Locate every blood parasite and identify its species.
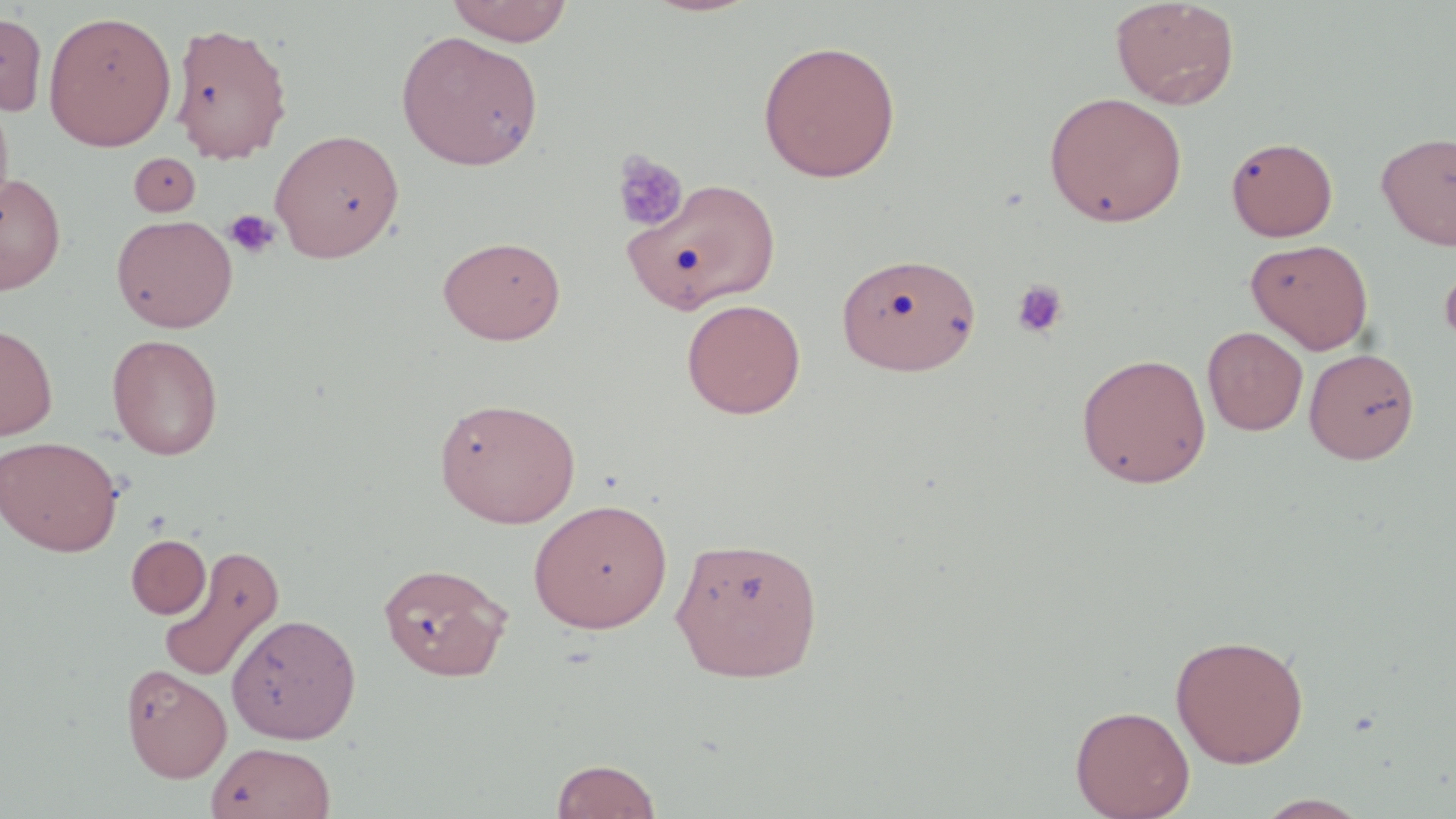
No blood parasites observed.

Summary:
  - Coordinate format: approximate bounding boxes as [x1, y1, x2, y2] in pixels
  - Uninfected red blood cell locations: [446, 0, 573, 46], [1109, 0, 1241, 110], [44, 10, 176, 151], [0, 12, 48, 116], [170, 21, 293, 163], [396, 30, 544, 170], [758, 40, 902, 183], [1043, 91, 1188, 228], [0, 92, 14, 218], [270, 128, 404, 263], [1376, 131, 1456, 251], [1225, 136, 1338, 241], [129, 152, 201, 216], [0, 172, 66, 294], [622, 176, 782, 313], [112, 214, 238, 333], [437, 235, 566, 345], [1245, 238, 1374, 354], [836, 252, 981, 376], [1438, 252, 1456, 351], [681, 298, 806, 419], [0, 322, 58, 440], [1202, 326, 1308, 436], [107, 333, 223, 460], [1304, 348, 1419, 463], [1076, 352, 1212, 489], [433, 396, 581, 528], [0, 435, 123, 556], [529, 498, 673, 633], [670, 533, 824, 683], [126, 534, 211, 618], [158, 544, 285, 682], [378, 561, 512, 681], [226, 613, 361, 744], [1170, 633, 1309, 768], [121, 663, 231, 781], [1070, 704, 1195, 819], [206, 741, 336, 819], [551, 758, 662, 818], [1252, 794, 1373, 818]
  - Platelet locations: [610, 149, 688, 232], [224, 209, 280, 259], [1010, 279, 1069, 340]
  - Slide-level diagnosis: no evidence of blood parasites
  - Preparation: thin blood smear
  - Stain: May-Grünwald-Giemsa
  - Modality: light microscopy
  - Image size: 1456×819 pixels
  - Field of view: single
  - Magnification: 1000x